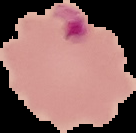

Summary:
  - Preparation: thin blood film
  - Image size: 136×133 pixels
  - Image type: segmented cell region with the area outside set to black
  - Result: malaria parasites detected